Locate and identify every blood parasite.
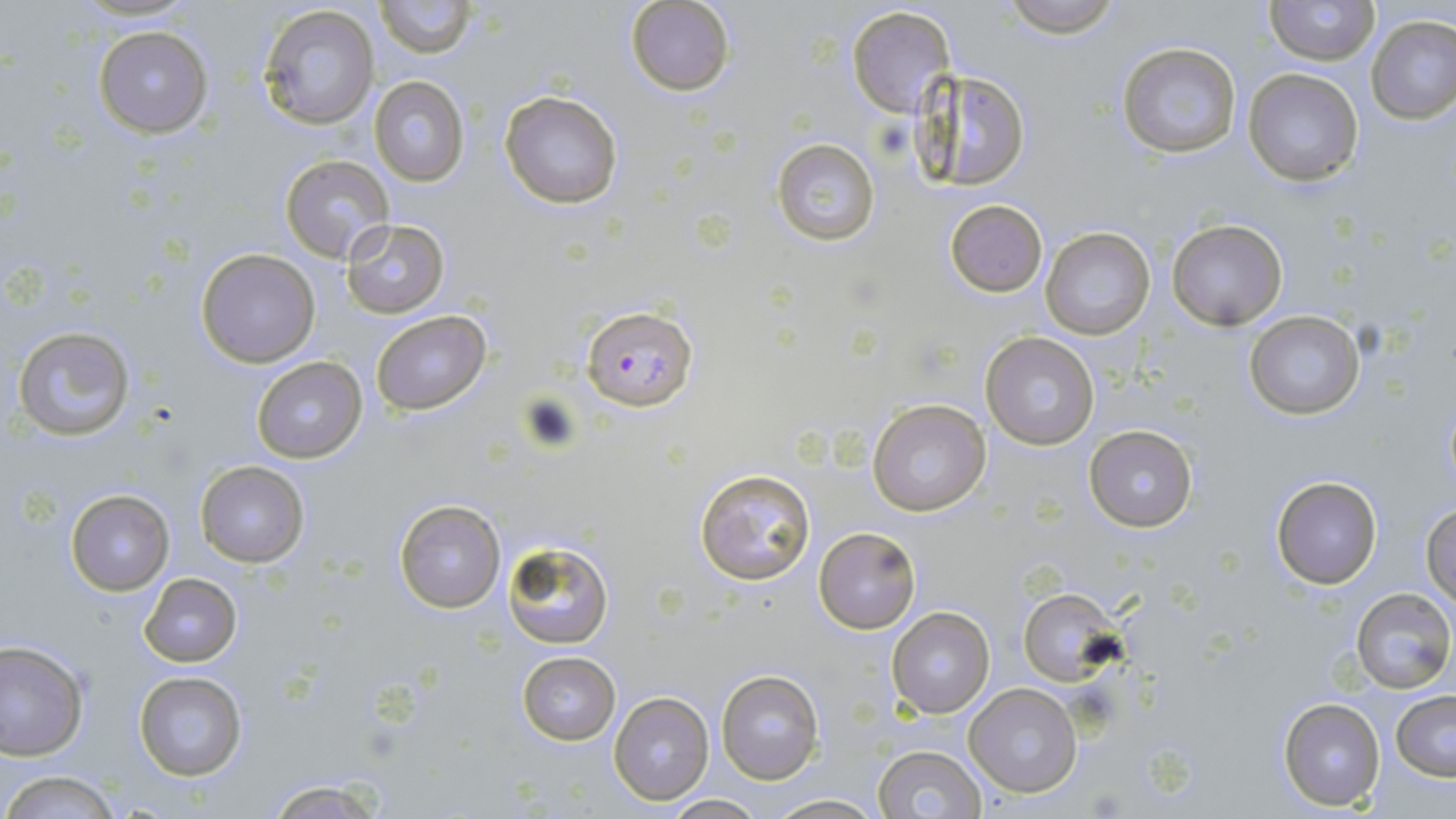

Approximate bounding boxes as (x1,y1)-(x2,y2) corner pairs in pixels.
Plasmodium falciparum-infected red blood cells: (583,306)-(697,410).
No Plasmodium ovale, Plasmodium malariae, Plasmodium vivax, Babesia divergens, or Trypanosoma brucei observed.

Uninfected red blood cell locations: (374,0)-(472,58), (998,0)-(1125,39), (1265,0)-(1380,66), (626,1)-(735,97), (846,5)-(956,118), (258,6)-(381,130), (1366,15)-(1456,123), (93,25)-(213,137), (1116,41)-(1242,159), (910,66)-(1032,190), (1244,67)-(1365,187), (369,75)-(469,185), (500,91)-(623,208), (772,138)-(882,246), (280,155)-(394,264), (946,199)-(1048,296), (1166,217)-(1289,331), (342,219)-(449,317), (1040,227)-(1156,341), (196,247)-(319,367), (371,310)-(491,415), (1244,311)-(1365,421), (12,325)-(135,441), (981,331)-(1100,450), (251,356)-(368,462), (867,398)-(992,517), (1084,425)-(1198,530), (195,461)-(309,567), (695,467)-(818,586), (1270,475)-(1382,589), (65,489)-(174,594), (392,499)-(507,615), (1422,505)-(1456,609), (814,527)-(921,633), (503,540)-(613,649), (139,573)-(242,667), (1018,587)-(1123,685), (1351,587)-(1454,692), (885,607)-(995,719), (0,641)-(90,760), (517,652)-(620,745), (134,670)-(247,781), (717,670)-(823,784), (965,682)-(1083,798), (608,690)-(715,805), (1391,691)-(1456,781), (1278,696)-(1385,811), (874,745)-(988,819), (1,770)-(126,818), (260,779)-(392,818), (662,794)-(764,818), (765,794)-(885,818). Slide-level diagnosis: Plasmodium falciparum. Optical microscopy. One field of a larger specimen. Image is 1456×819 pixels. Captured at 1000x magnification. May-Grünwald-Giemsa stain. Thin blood smear.